Assess this cell for malaria.
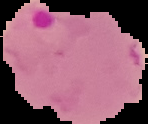

It is parasitized.

{
  "image_size": "148×124 pixels",
  "preparation": "thin blood smear",
  "image_type": "segmented cell region on a black background"
}